Name the parasite shown.
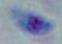
This is Toxoplasma gondii.

magnification = 1000x
modality = micrograph